Assess this cell for malaria.
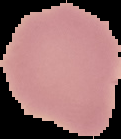

Uninfected.

{
  "image_type": "segmented cell region on a black background",
  "preparation": "thin blood smear",
  "image_size": "121×139 pixels"
}